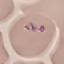
Summary:
  - Result: malaria parasites detected
  - Capture: smartphone through the microscope eyepiece
  - Image type: automatically extracted cell patch, resized to 64 × 64 pixels
  - Stain: Giemsa
  - Preparation: thin blood film